Give the extent of all uninfected red blood cells.
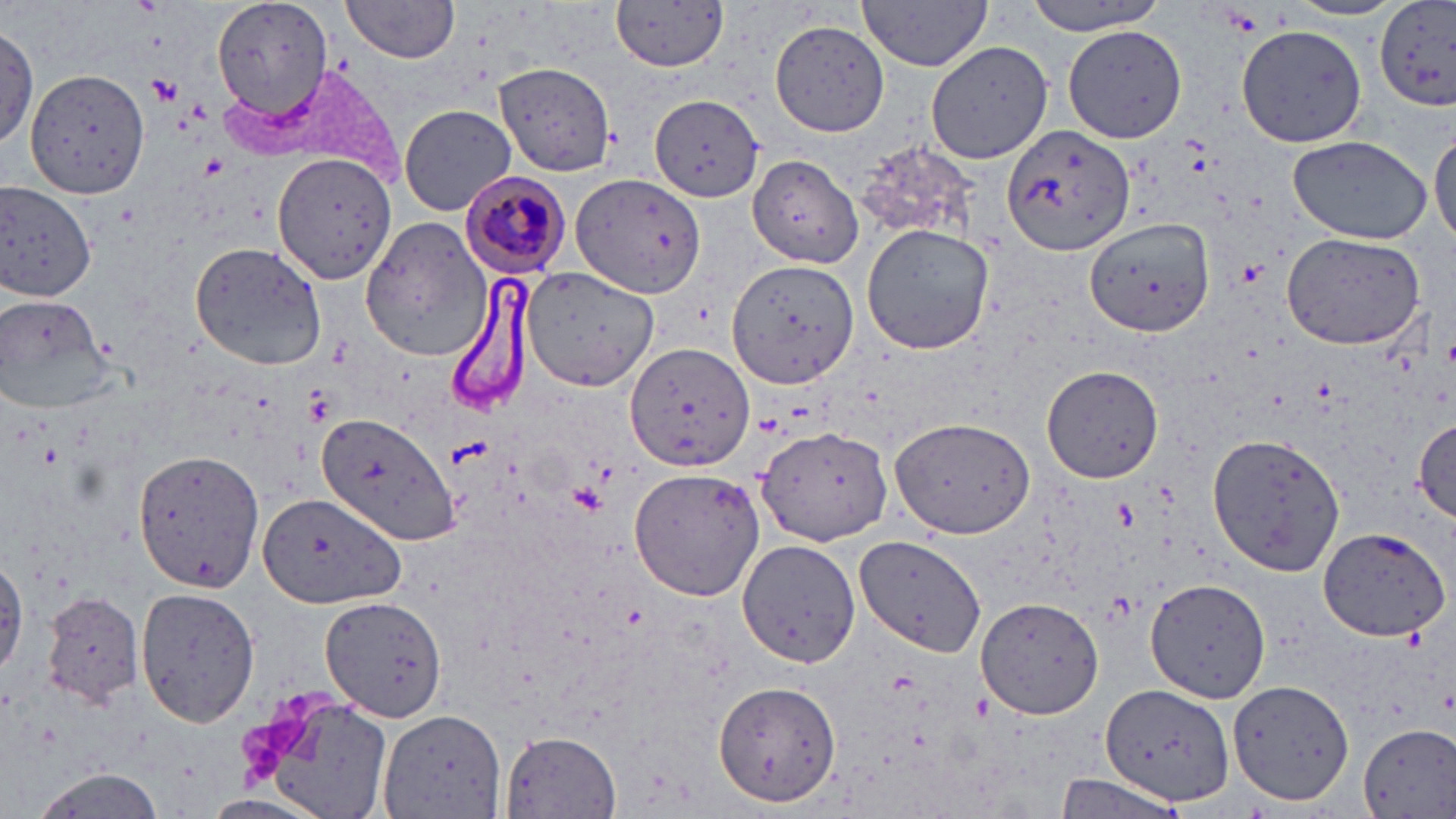

Approximate bounding boxes as (x1, y1, x2, y2) in pixels.
Uninfected red blood cells: (208, 0, 333, 123), (612, 0, 729, 73), (858, 0, 995, 70), (1022, 0, 1174, 34), (1281, 0, 1406, 21), (339, 1, 458, 65), (1376, 3, 1456, 113), (770, 21, 888, 135), (1, 22, 39, 154), (1062, 25, 1188, 144), (1238, 26, 1366, 147), (926, 39, 1055, 166), (495, 62, 615, 177), (28, 70, 150, 198), (649, 94, 766, 201), (399, 104, 517, 216), (1002, 125, 1138, 256), (1430, 125, 1455, 248), (1286, 135, 1433, 242), (850, 144, 983, 251), (273, 153, 398, 284), (749, 155, 864, 270), (572, 174, 706, 299), (0, 180, 98, 303), (1086, 217, 1216, 336), (359, 219, 490, 362), (861, 225, 995, 357), (1282, 233, 1425, 351), (187, 240, 332, 373), (725, 258, 859, 392), (523, 266, 659, 391), (0, 295, 113, 413), (621, 340, 752, 474), (1041, 363, 1165, 483), (316, 409, 461, 548), (891, 417, 1036, 536), (1409, 418, 1456, 522), (757, 428, 893, 545), (1208, 432, 1346, 578), (133, 448, 264, 592), (629, 466, 764, 602), (257, 489, 407, 608), (1317, 528, 1451, 643), (859, 537, 985, 659), (734, 539, 860, 667), (1, 557, 26, 679), (1146, 578, 1271, 702), (136, 584, 262, 728), (39, 589, 146, 711), (321, 594, 451, 721), (976, 594, 1106, 721), (1230, 680, 1353, 804), (715, 681, 841, 804), (1099, 682, 1235, 807), (238, 684, 394, 817), (381, 711, 506, 818), (1359, 723, 1456, 818), (499, 728, 621, 818), (25, 768, 166, 819), (1050, 774, 1184, 817).

Summary:
  - Platelet locations: (1225, 8, 1264, 35), (149, 74, 183, 103), (1237, 257, 1268, 285), (303, 391, 334, 425), (567, 484, 606, 514)
  - Plasmodium malariae-infected red blood cell locations: (460, 170, 573, 278)
  - Slide-level diagnosis: Plasmodium malariae
  - Magnification: 1000x
  - Image size: 1456×819 pixels
  - Modality: light microscopy
  - Stain: May-Grünwald-Giemsa
  - Field of view: one of a larger specimen
  - Preparation: thin blood smear